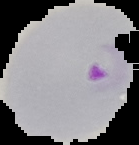 From a thin blood film. Cell region segmented out of the field of view; the surrounding area is masked to black. Malaria status: parasitized. Image is 139×145 pixels.